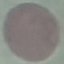
malaria status = uninfected
stain = Giemsa
image type = automatically extracted cell patch, resized to 64 × 64 pixels
capture = smartphone camera at the microscope eyepiece
preparation = thin smear